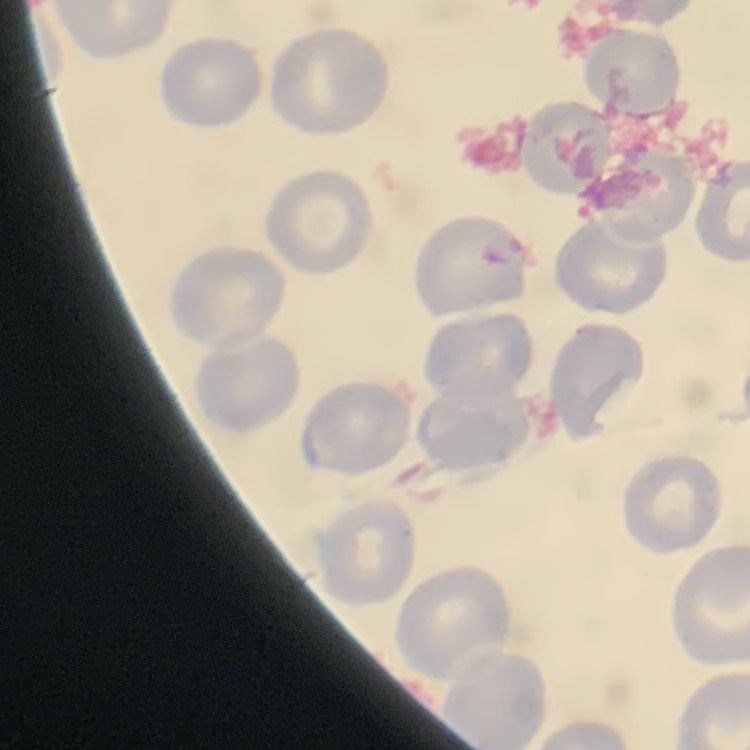
The red blood cells exhibit no rouleaux formation. Field's or Giemsa stain. Thin peripheral smear. Square crop of a larger photomicrograph.